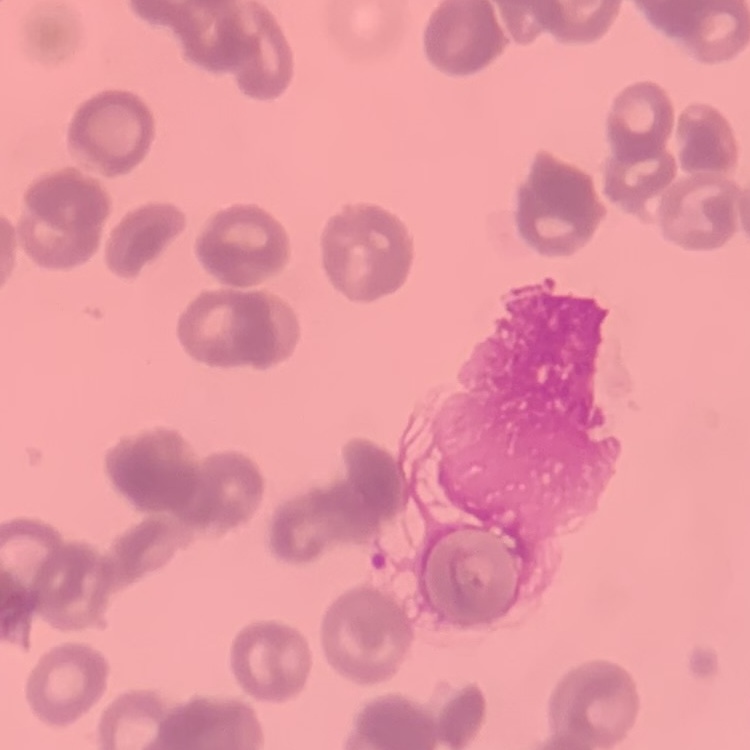

The erythrocytes exhibit rouleaux formation. Field's or Giemsa stain. Thin peripheral smear. One tile cut from a larger photomicrograph.